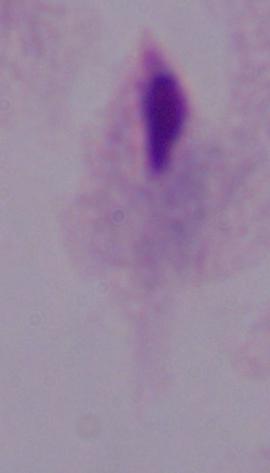

Summary:
  - Identification: trichomonad
  - Magnification: 1000x
  - Modality: micrograph